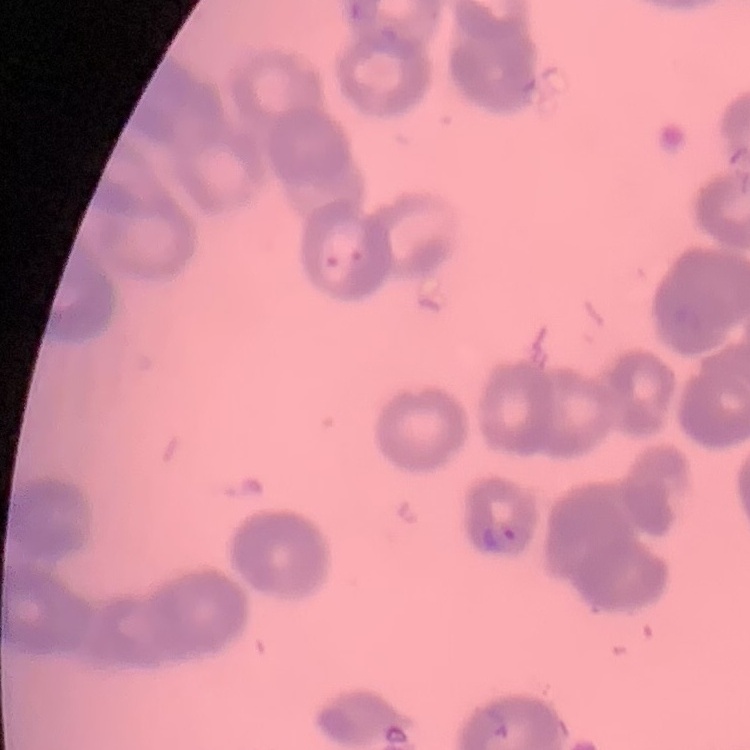 The erythrocytes exhibit rouleaux formation. Square crop of a larger photomicrograph. Thin peripheral smear. Stained with either Field's or Giemsa.